Assess this cell for malaria.
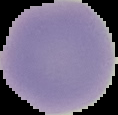
Uninfected.

From a thin blood film. Segmented cell region on a black background. Image is 118×115 pixels.